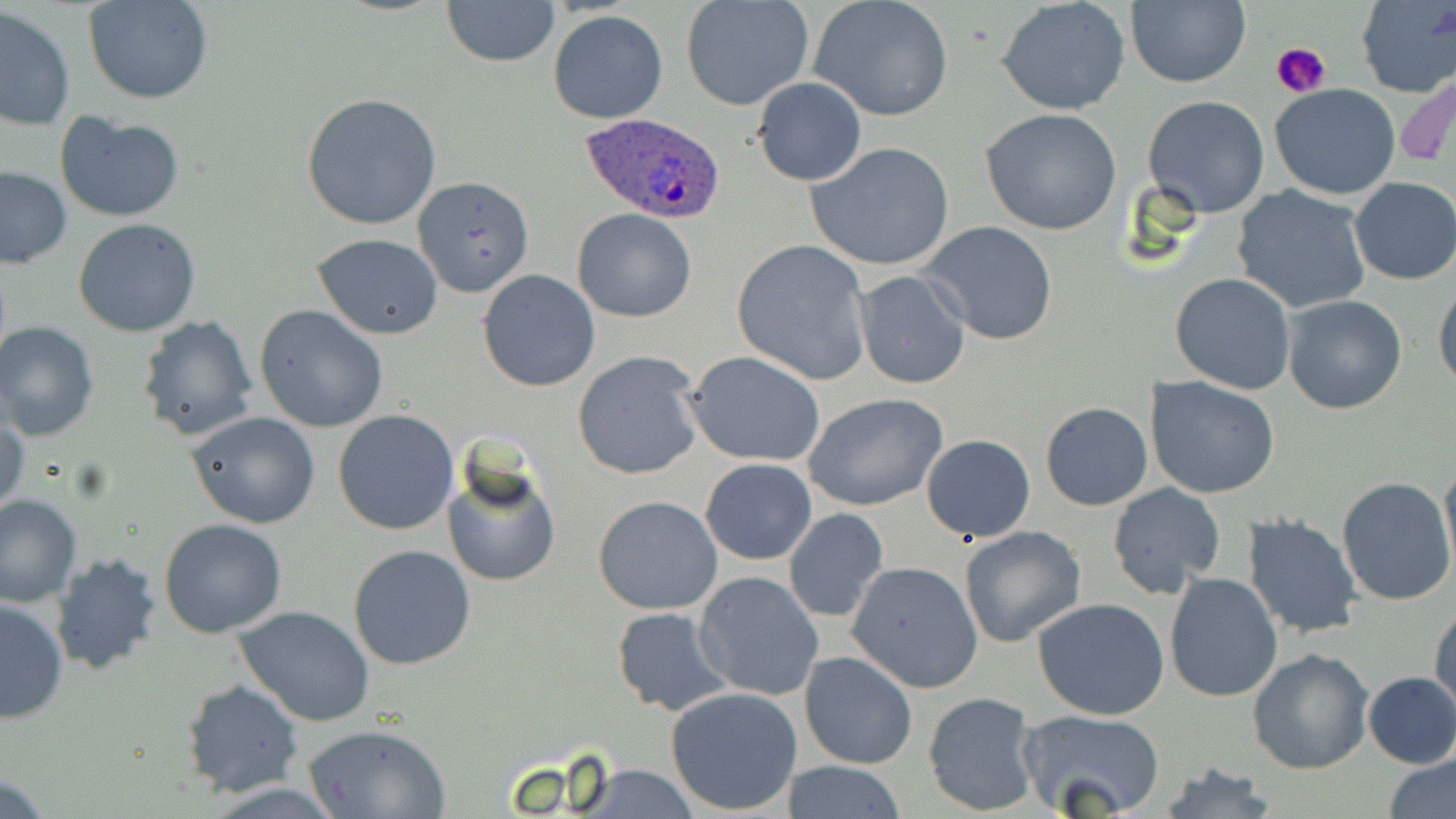

slide-level diagnosis = Plasmodium ovale
field of view = single
uninfected red blood cell locations = approximate bounding boxes as named x1/y1/x2/y2 corners in pixels: (x1=85, y1=0, x2=213, y2=104), (x1=441, y1=0, x2=560, y2=68), (x1=680, y1=0, x2=815, y2=112), (x1=809, y1=0, x2=954, y2=122), (x1=997, y1=0, x2=1131, y2=116), (x1=1125, y1=0, x2=1251, y2=88), (x1=1356, y1=0, x2=1456, y2=98), (x1=1, y1=7, x2=75, y2=131), (x1=549, y1=11, x2=669, y2=124), (x1=1397, y1=74, x2=1456, y2=172), (x1=752, y1=78, x2=867, y2=186), (x1=1269, y1=83, x2=1402, y2=200), (x1=302, y1=92, x2=442, y2=231), (x1=1142, y1=95, x2=1271, y2=218), (x1=980, y1=108, x2=1124, y2=235), (x1=54, y1=110, x2=186, y2=223), (x1=807, y1=142, x2=956, y2=271), (x1=0, y1=166, x2=72, y2=268), (x1=412, y1=174, x2=534, y2=299), (x1=1350, y1=177, x2=1456, y2=285), (x1=1231, y1=186, x2=1371, y2=314), (x1=573, y1=209, x2=696, y2=323), (x1=73, y1=218, x2=202, y2=337), (x1=919, y1=222, x2=1061, y2=348), (x1=314, y1=235, x2=443, y2=339), (x1=732, y1=238, x2=874, y2=386), (x1=476, y1=270, x2=600, y2=391), (x1=851, y1=270, x2=972, y2=391), (x1=1169, y1=272, x2=1296, y2=394), (x1=1433, y1=280, x2=1456, y2=393), (x1=1280, y1=295, x2=1408, y2=415), (x1=253, y1=304, x2=389, y2=432), (x1=136, y1=315, x2=260, y2=442), (x1=0, y1=321, x2=100, y2=440), (x1=573, y1=350, x2=704, y2=480), (x1=683, y1=351, x2=827, y2=466), (x1=1146, y1=375, x2=1281, y2=499), (x1=804, y1=392, x2=948, y2=512), (x1=1040, y1=402, x2=1153, y2=512), (x1=332, y1=409, x2=459, y2=535), (x1=1, y1=411, x2=29, y2=521), (x1=187, y1=411, x2=323, y2=528), (x1=921, y1=433, x2=1036, y2=542), (x1=1440, y1=456, x2=1456, y2=577), (x1=701, y1=458, x2=816, y2=565), (x1=442, y1=460, x2=561, y2=589), (x1=1336, y1=478, x2=1455, y2=606), (x1=1106, y1=483, x2=1226, y2=598), (x1=0, y1=494, x2=82, y2=607), (x1=593, y1=494, x2=723, y2=615), (x1=784, y1=508, x2=891, y2=625), (x1=1242, y1=514, x2=1364, y2=640), (x1=158, y1=519, x2=287, y2=638), (x1=958, y1=525, x2=1086, y2=648), (x1=349, y1=545, x2=477, y2=668), (x1=50, y1=551, x2=163, y2=676), (x1=846, y1=560, x2=983, y2=693), (x1=693, y1=572, x2=825, y2=702), (x1=1163, y1=572, x2=1285, y2=703), (x1=0, y1=596, x2=69, y2=721), (x1=1032, y1=598, x2=1173, y2=720), (x1=1430, y1=601, x2=1455, y2=718), (x1=235, y1=605, x2=375, y2=727), (x1=610, y1=607, x2=732, y2=715), (x1=1247, y1=648, x2=1374, y2=774), (x1=799, y1=650, x2=919, y2=770), (x1=1361, y1=672, x2=1456, y2=767), (x1=181, y1=679, x2=304, y2=797), (x1=666, y1=687, x2=803, y2=815), (x1=922, y1=690, x2=1040, y2=815), (x1=1018, y1=709, x2=1168, y2=819), (x1=301, y1=724, x2=450, y2=818), (x1=1382, y1=751, x2=1455, y2=819), (x1=785, y1=760, x2=908, y2=817), (x1=1154, y1=761, x2=1279, y2=819), (x1=566, y1=764, x2=707, y2=818)
Plasmodium ovale-infected red blood cell locations = approximate bounding boxes as named x1/y1/x2/y2 corners in pixels: (x1=578, y1=111, x2=727, y2=223)
modality = light microscopy
preparation = thin blood smear
magnification = 1000x
stain = May-Grünwald-Giemsa
image size = 1456×819 pixels
platelet locations = approximate bounding boxes as named x1/y1/x2/y2 corners in pixels: (x1=1272, y1=41, x2=1333, y2=100)